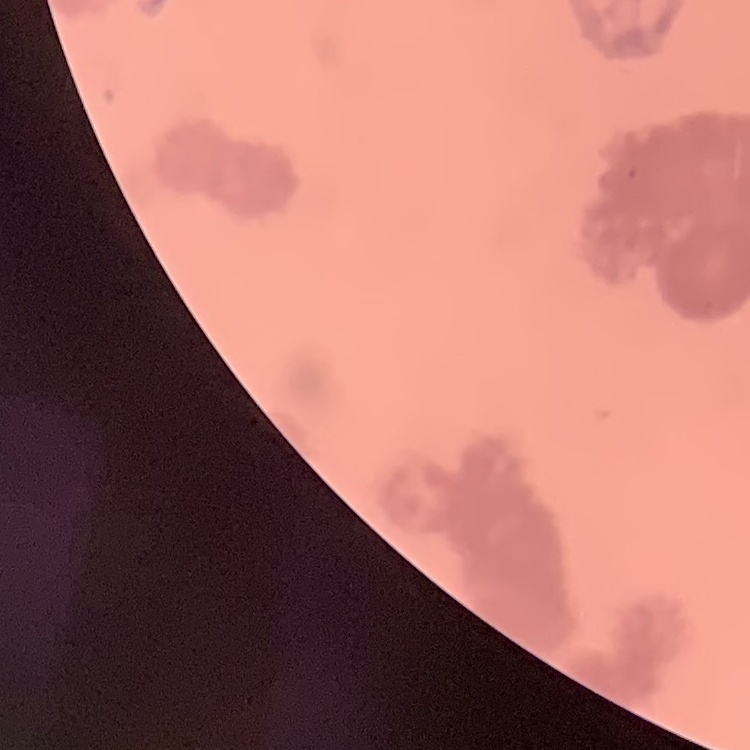

The erythrocytes exhibit rouleaux formation. Thin peripheral smear. Stained with either Field's or Giemsa. One tile cut from a larger photomicrograph.